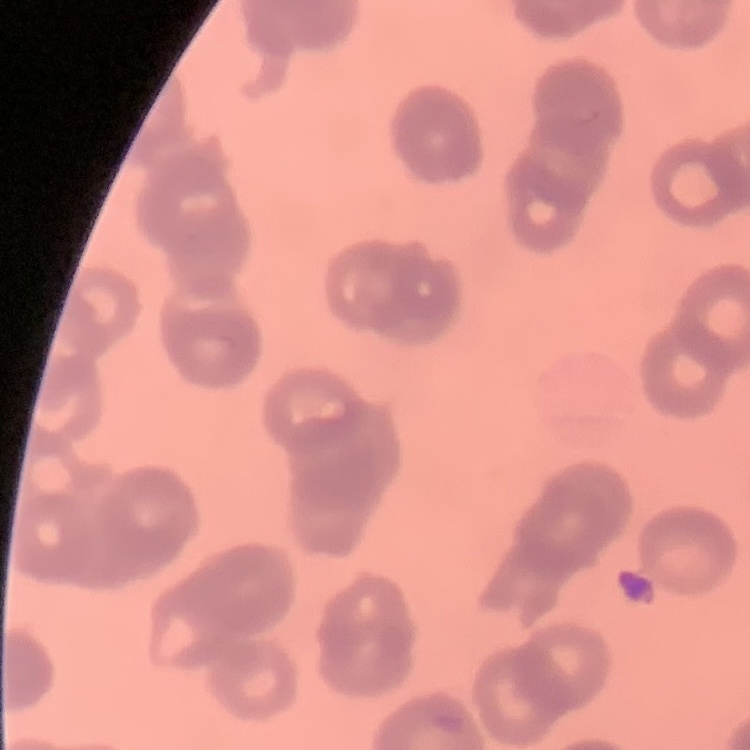
Summary:
  - Erythrocyte morphology: rouleaux formation
  - Stain: Field's or Giemsa
  - Image type: square crop of a larger photomicrograph
  - Preparation: thin blood film